Report the malaria status of this cell.
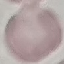
Uninfected.

Automatically extracted cell patch, resized to 64 × 64 pixels. Giemsa stain. Photographed with a smartphone camera at the microscope eyepiece. Thin blood film.